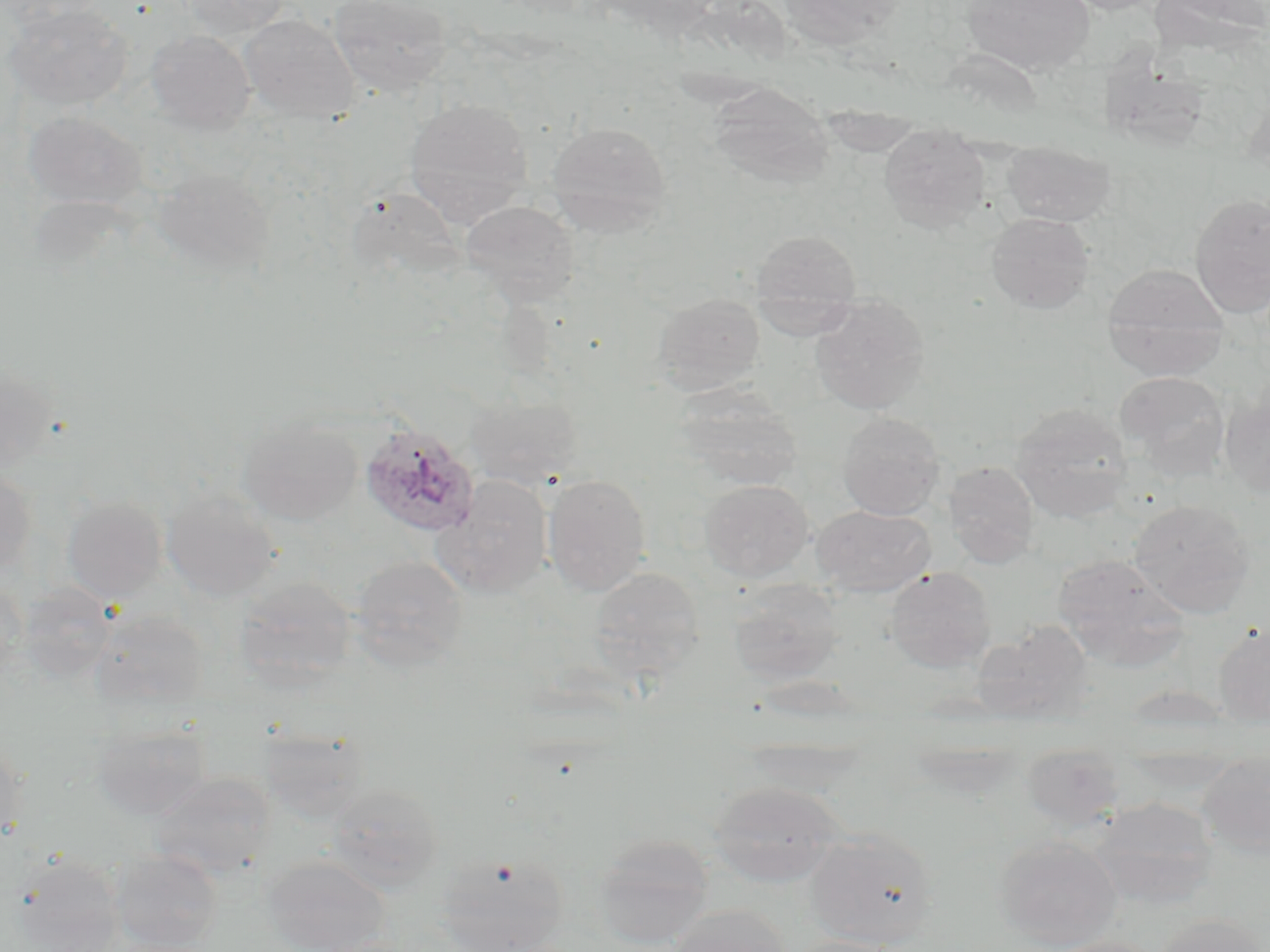 Approximate bounding boxes as named x1/y1/x2/y2 corners in pixels. Plasmodium ovale-infected red blood cell locations: (x1=360, y1=424, x2=480, y2=537). Uninfected red blood cell locations: (x1=182, y1=0, x2=291, y2=39), (x1=328, y1=0, x2=453, y2=97), (x1=778, y1=0, x2=907, y2=50), (x1=962, y1=0, x2=1096, y2=76), (x1=2, y1=3, x2=133, y2=111), (x1=239, y1=14, x2=359, y2=122), (x1=145, y1=29, x2=255, y2=134), (x1=1100, y1=35, x2=1200, y2=166), (x1=708, y1=84, x2=833, y2=190), (x1=404, y1=97, x2=533, y2=224), (x1=23, y1=111, x2=147, y2=209), (x1=545, y1=121, x2=672, y2=235), (x1=878, y1=124, x2=991, y2=232), (x1=1001, y1=140, x2=1116, y2=226), (x1=154, y1=166, x2=275, y2=275), (x1=349, y1=185, x2=463, y2=280), (x1=1190, y1=193, x2=1270, y2=317), (x1=461, y1=200, x2=579, y2=306), (x1=986, y1=213, x2=1094, y2=314), (x1=750, y1=229, x2=862, y2=315), (x1=1101, y1=263, x2=1230, y2=381), (x1=652, y1=293, x2=765, y2=393), (x1=809, y1=295, x2=931, y2=414), (x1=0, y1=362, x2=57, y2=474), (x1=1116, y1=372, x2=1231, y2=479), (x1=673, y1=385, x2=800, y2=490), (x1=1219, y1=385, x2=1270, y2=500), (x1=466, y1=391, x2=581, y2=489), (x1=1010, y1=404, x2=1132, y2=523), (x1=837, y1=412, x2=946, y2=519), (x1=239, y1=418, x2=361, y2=525), (x1=944, y1=461, x2=1039, y2=568), (x1=0, y1=469, x2=37, y2=575), (x1=543, y1=474, x2=651, y2=595), (x1=435, y1=475, x2=553, y2=596), (x1=700, y1=479, x2=814, y2=581), (x1=161, y1=489, x2=282, y2=601), (x1=62, y1=496, x2=168, y2=602), (x1=1130, y1=499, x2=1256, y2=618), (x1=812, y1=505, x2=935, y2=596), (x1=351, y1=554, x2=468, y2=668), (x1=1052, y1=554, x2=1189, y2=671), (x1=588, y1=566, x2=706, y2=679), (x1=885, y1=566, x2=995, y2=672), (x1=234, y1=576, x2=357, y2=688), (x1=727, y1=578, x2=843, y2=685), (x1=0, y1=579, x2=27, y2=679), (x1=17, y1=582, x2=116, y2=683), (x1=90, y1=608, x2=210, y2=711), (x1=973, y1=621, x2=1094, y2=725), (x1=1213, y1=623, x2=1270, y2=726), (x1=92, y1=721, x2=212, y2=820), (x1=263, y1=726, x2=369, y2=823), (x1=0, y1=734, x2=28, y2=842), (x1=740, y1=735, x2=869, y2=798), (x1=1021, y1=742, x2=1125, y2=830), (x1=1198, y1=752, x2=1270, y2=858), (x1=151, y1=771, x2=272, y2=880), (x1=326, y1=781, x2=444, y2=891), (x1=709, y1=781, x2=844, y2=887), (x1=1088, y1=796, x2=1217, y2=909), (x1=805, y1=828, x2=940, y2=948), (x1=594, y1=832, x2=714, y2=948), (x1=993, y1=834, x2=1122, y2=949), (x1=110, y1=849, x2=223, y2=951), (x1=435, y1=851, x2=569, y2=952), (x1=8, y1=855, x2=125, y2=951), (x1=262, y1=855, x2=393, y2=952), (x1=667, y1=903, x2=792, y2=952), (x1=1154, y1=914, x2=1269, y2=952), (x1=782, y1=936, x2=907, y2=952), (x1=1042, y1=936, x2=1165, y2=952). Slide-level diagnosis: Plasmodium ovale. Light microscopy. May-Grünwald-Giemsa-stained preparation. Captured at 1000x magnification. Thin blood film. Single field of view. Image is 1270×952 pixels.